State which parasite is depicted.
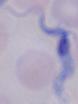
A trypanosome.

Micrograph. 1000x magnification.